Give the preparation type.
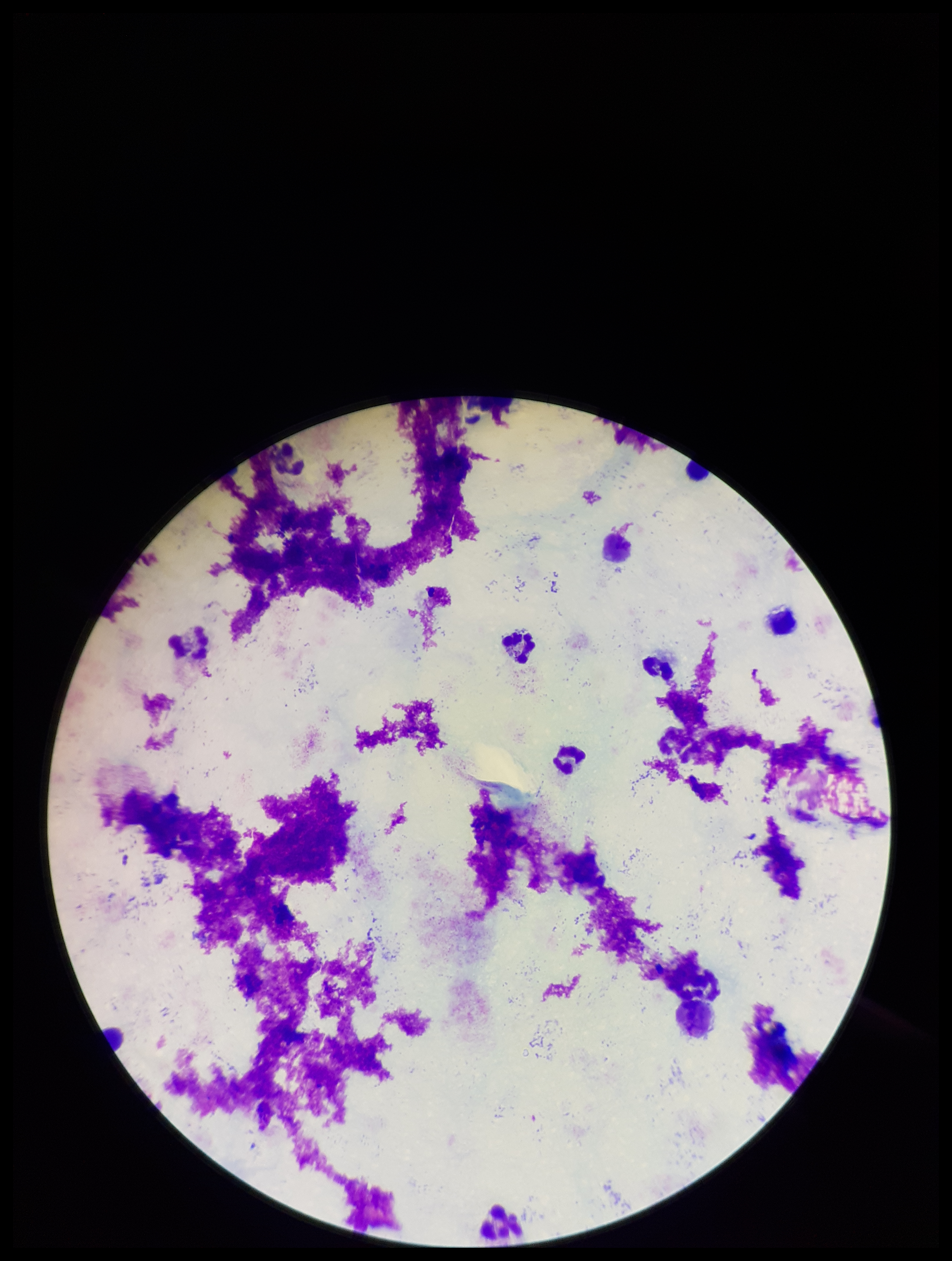

Thick.

Giemsa stain. Leukocyte count: 9. Image is 952×1261 pixels. Plasmodium parasites: none seen. Parasite count: 0. One field from this slide. Patient malaria status: negative. Smartphone photograph taken through the eyepiece of a microscope.